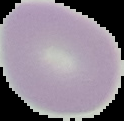
Cell region segmented out of the field of view; the surrounding area is masked to black. Result: no Plasmodium parasites seen. Image is 124×121 pixels. From a thin blood film.